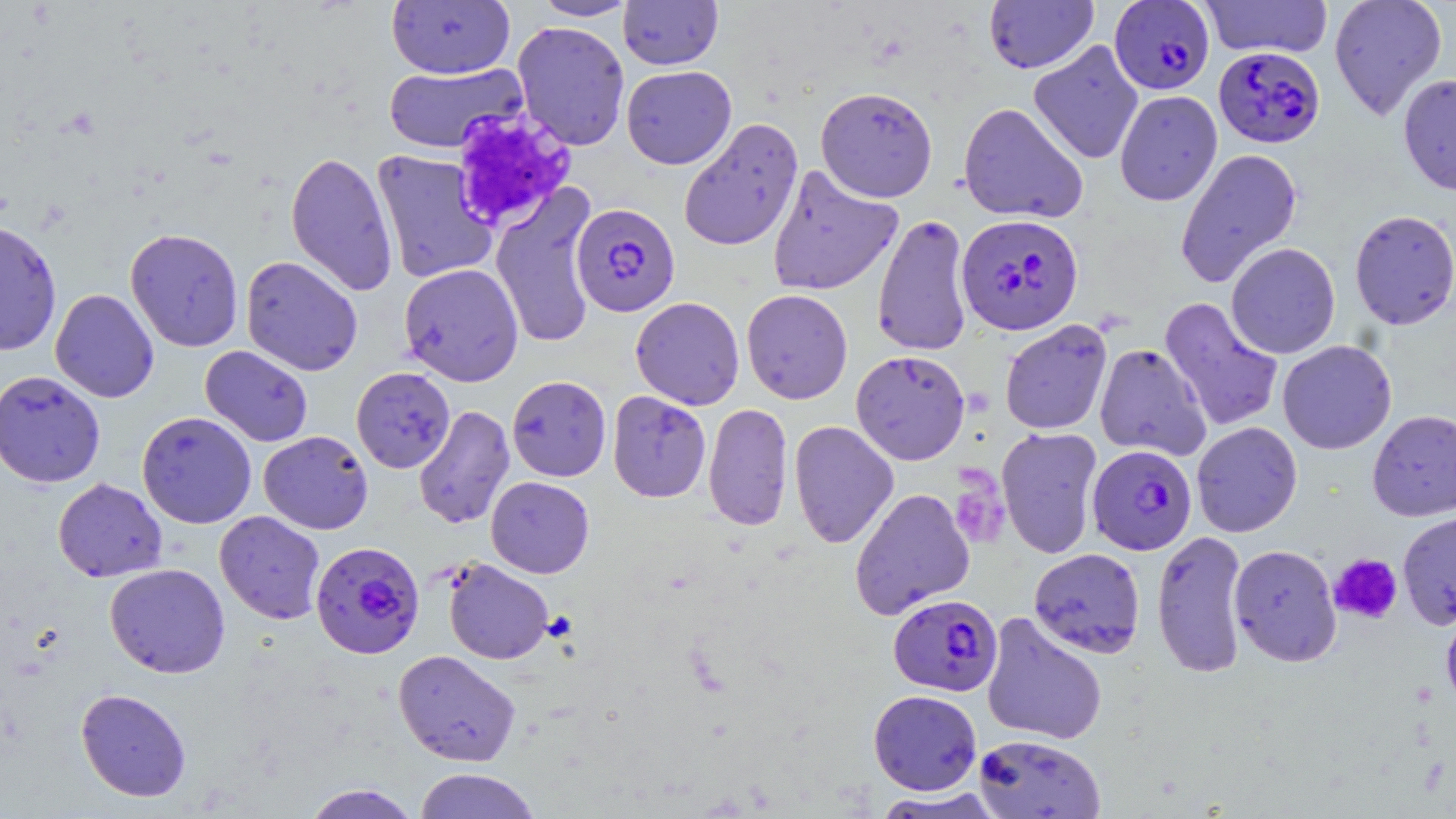

slide-level diagnosis = Plasmodium falciparum
stain = May-Grünwald-Giemsa
preparation = thin blood film
image size = 1456×819 pixels
modality = optical microscopy
uninfected red blood cell locations = approximate bounding boxes as (x1, y1, x2, y2) in pixels: (532, 0, 638, 21), (618, 0, 723, 70), (983, 0, 1098, 74), (1200, 0, 1333, 59), (1329, 0, 1447, 122), (386, 1, 515, 79), (512, 21, 630, 151), (1028, 40, 1144, 165), (383, 63, 526, 154), (621, 65, 736, 169), (1398, 72, 1456, 197), (815, 85, 938, 202), (1115, 90, 1222, 206), (958, 102, 1088, 224), (678, 118, 803, 252), (1175, 147, 1303, 287), (370, 149, 498, 284), (285, 151, 398, 297), (767, 165, 903, 297), (491, 184, 598, 349), (1349, 209, 1456, 330), (872, 213, 973, 357), (0, 219, 62, 357), (125, 227, 244, 352), (1225, 242, 1341, 359), (240, 256, 363, 376), (400, 263, 524, 386), (50, 288, 159, 403), (741, 289, 853, 404), (630, 297, 745, 410), (1159, 297, 1284, 433), (999, 319, 1112, 435), (1277, 339, 1397, 455), (1094, 343, 1212, 461), (200, 345, 313, 447), (851, 350, 970, 465), (351, 367, 455, 473), (0, 370, 106, 488), (507, 375, 612, 482), (607, 390, 711, 502), (703, 403, 794, 531), (413, 405, 515, 530), (1367, 409, 1456, 521), (137, 411, 256, 528), (788, 420, 899, 549), (1191, 421, 1302, 537), (996, 427, 1103, 559), (259, 430, 373, 534), (485, 476, 595, 578), (52, 478, 167, 582), (849, 487, 975, 620), (1397, 510, 1456, 630), (215, 511, 326, 624), (1151, 528, 1249, 679), (1228, 543, 1342, 667), (1028, 547, 1145, 658), (442, 559, 554, 664), (104, 563, 230, 678), (1440, 598, 1456, 718), (981, 612, 1108, 746), (393, 649, 521, 766), (75, 687, 192, 802), (868, 689, 982, 795), (973, 733, 1105, 818), (413, 768, 542, 818), (302, 783, 422, 819), (871, 788, 1007, 818)
magnification = 1000x
platelet locations = approximate bounding boxes as (x1, y1, x2, y2) in pixels: (449, 108, 577, 232), (951, 464, 1008, 545), (1329, 554, 1402, 624)
field of view = one of a larger specimen
Plasmodium falciparum-infected red blood cell locations = approximate bounding boxes as (x1, y1, x2, y2) in pixels: (1110, 0, 1214, 94), (1214, 46, 1325, 148), (571, 202, 680, 317), (956, 213, 1083, 335), (1087, 444, 1197, 555), (310, 540, 425, 659), (888, 594, 1003, 697)